Classify this cell by malaria status.
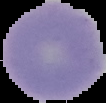
Uninfected.

image type = cell region segmented out of the field of view; surrounding area masked to black
image size = 106×103 pixels
preparation = thin blood smear